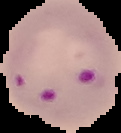
image type = segmented cell region with the area outside set to black
image size = 121×133 pixels
malaria status = parasitized
preparation = thin blood film